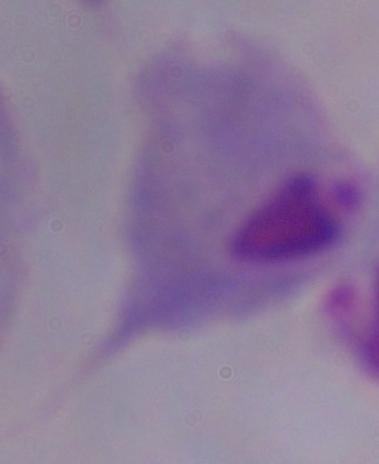 A trichomonad is seen. Photomicrograph. Captured at 1000x magnification.